Comment on the morphology of the erythrocytes.
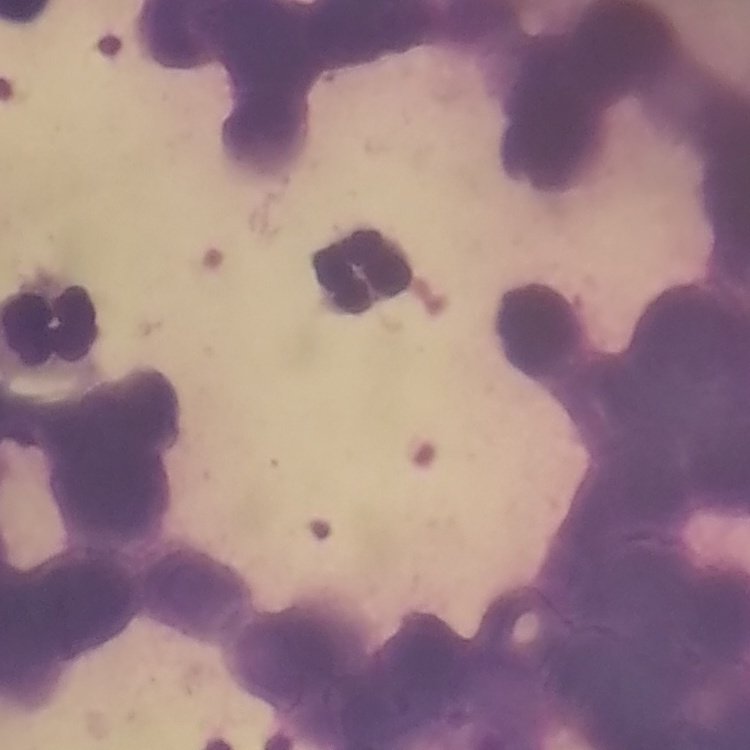
Rouleaux formation.

stain = Field's or Giemsa
preparation = thin peripheral smear
image type = square crop of a larger photomicrograph